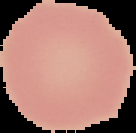 Image is 136×133 pixels. Result: negative for Plasmodium parasites. The area outside the segmented cell region is set to black. From a thin blood smear.